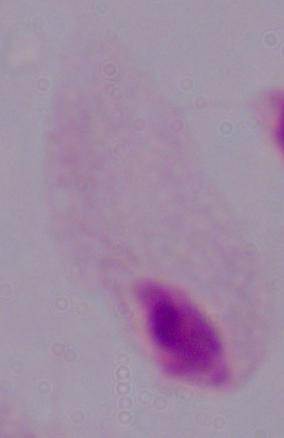
A trichomonad is shown. 1000x magnification. Micrograph.